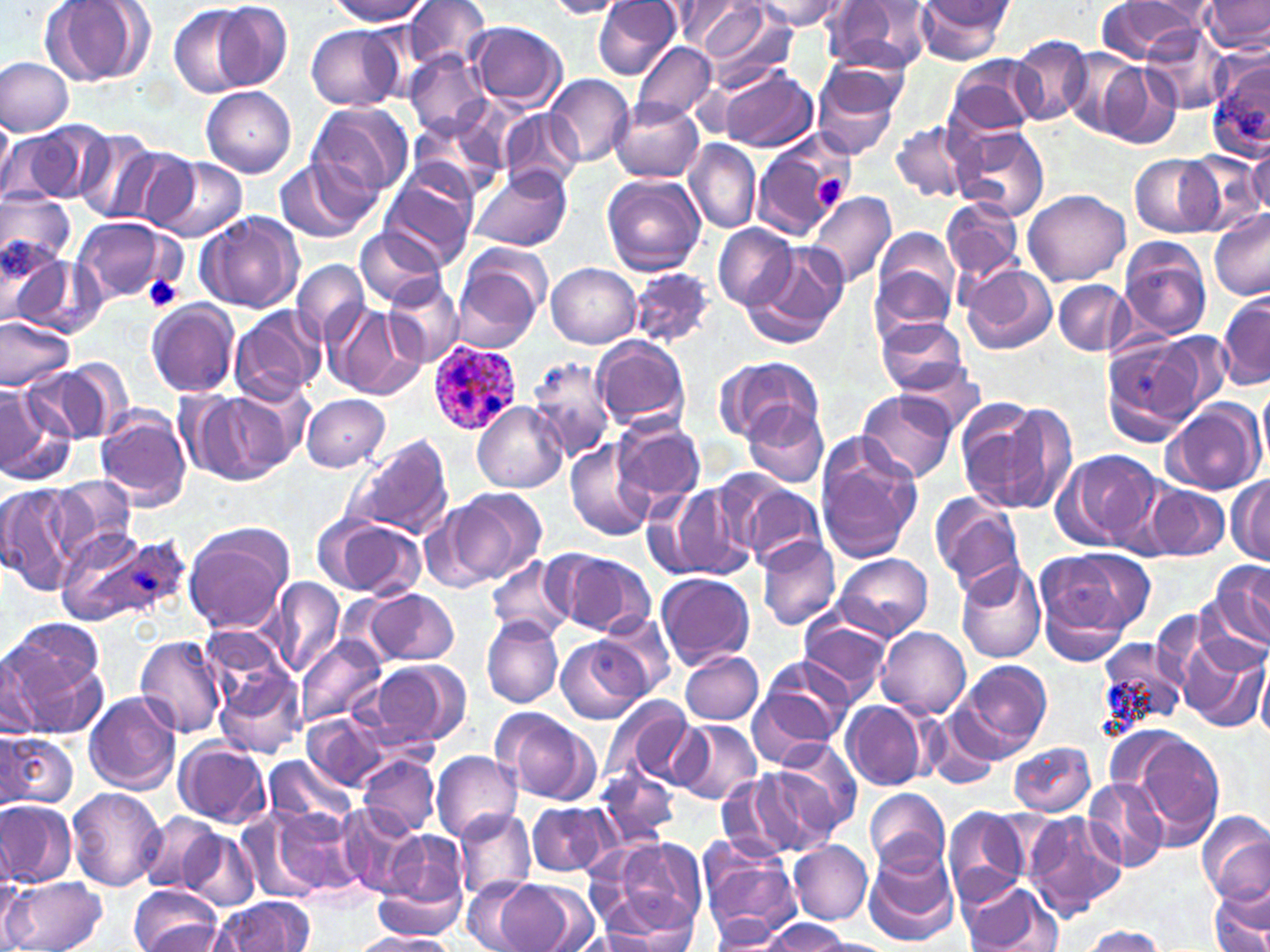
{
  "slide_level_diagnosis": "Plasmodium ovale",
  "modality": "optical microscopy",
  "uninfected_red_blood_cell_locations": "approximate bounding boxes as (x1, y1, x2, y2) in pixels: (204, 0, 293, 90), (327, 0, 431, 25), (403, 0, 491, 69), (753, 0, 847, 30), (821, 0, 930, 76), (913, 0, 1014, 65), (1203, 0, 1269, 53), (39, 1, 154, 86), (543, 1, 634, 18), (593, 1, 680, 79), (666, 2, 764, 51), (1095, 2, 1201, 61), (696, 3, 795, 86), (169, 5, 259, 97), (467, 20, 567, 110), (305, 24, 407, 111), (1141, 24, 1231, 115), (1011, 37, 1094, 124), (632, 40, 720, 123), (819, 50, 912, 121), (1062, 50, 1148, 137), (405, 51, 490, 139), (1207, 52, 1270, 158), (945, 55, 1044, 139), (0, 57, 72, 137), (1086, 59, 1181, 148), (721, 65, 818, 151), (812, 71, 902, 161), (545, 75, 633, 168), (201, 85, 297, 178), (308, 100, 414, 200), (610, 100, 703, 183), (501, 109, 582, 193), (0, 111, 14, 197), (407, 113, 507, 199), (891, 119, 974, 203), (2, 123, 104, 205), (952, 125, 1050, 222), (73, 129, 163, 225), (753, 132, 857, 239), (1246, 136, 1270, 219), (685, 139, 760, 233), (109, 143, 198, 230), (1186, 153, 1264, 235), (1130, 154, 1222, 237), (152, 158, 246, 244), (274, 159, 370, 243), (380, 164, 479, 267), (469, 165, 571, 254), (601, 174, 707, 275), (1023, 188, 1132, 285), (1, 192, 74, 272), (806, 192, 896, 287), (943, 197, 1022, 284), (948, 202, 1035, 353), (1208, 209, 1270, 302), (196, 212, 304, 313), (73, 216, 177, 305), (714, 223, 799, 311), (873, 227, 962, 328), (355, 228, 447, 307), (1119, 237, 1213, 342), (2, 241, 75, 332), (741, 242, 849, 348), (452, 250, 549, 352), (18, 257, 107, 340), (293, 259, 371, 348), (547, 263, 641, 348), (959, 264, 1057, 355), (630, 267, 715, 347), (385, 276, 465, 367), (1054, 280, 1131, 357), (1216, 292, 1270, 390), (145, 300, 240, 398), (327, 304, 426, 401), (229, 306, 325, 405), (0, 315, 75, 390), (873, 316, 970, 395), (1153, 333, 1238, 409), (592, 335, 691, 430), (1104, 339, 1200, 444), (527, 354, 615, 461), (715, 354, 823, 444), (60, 355, 134, 440), (893, 361, 988, 435), (26, 365, 114, 444), (0, 384, 68, 483), (856, 390, 959, 484), (188, 392, 292, 484), (301, 395, 390, 472), (955, 397, 1070, 517), (1161, 399, 1265, 497), (472, 401, 567, 493), (744, 402, 829, 488), (96, 411, 192, 510), (611, 418, 705, 511), (348, 434, 454, 542), (813, 435, 923, 564), (565, 442, 654, 542), (1054, 449, 1162, 550), (1228, 474, 1269, 564), (45, 476, 137, 566), (729, 478, 825, 568), (0, 481, 78, 594), (658, 483, 758, 583), (1145, 483, 1229, 561), (444, 488, 546, 586), (931, 493, 1026, 593), (320, 516, 426, 600), (184, 523, 295, 634), (756, 535, 842, 631), (548, 550, 657, 638), (1032, 550, 1144, 659), (834, 552, 933, 641), (487, 559, 573, 640), (955, 559, 1047, 663), (1210, 563, 1269, 650), (656, 572, 755, 670), (264, 578, 346, 679), (362, 588, 459, 666), (594, 611, 677, 699), (798, 611, 895, 701), (481, 615, 563, 708), (876, 626, 970, 717), (1180, 630, 1266, 731), (135, 635, 228, 738), (294, 635, 387, 731), (1096, 636, 1189, 735), (556, 637, 648, 723), (4, 640, 108, 741), (4, 649, 48, 739), (680, 651, 765, 725), (753, 657, 855, 749), (1255, 657, 1270, 740), (367, 659, 471, 749), (951, 659, 1053, 762), (215, 663, 308, 760), (747, 689, 840, 770), (84, 692, 182, 794), (598, 694, 697, 792), (842, 701, 929, 791), (492, 707, 601, 806), (919, 709, 1001, 792), (302, 714, 388, 791), (669, 720, 764, 806), (1128, 731, 1225, 845), (0, 732, 76, 812), (768, 738, 861, 840), (174, 741, 271, 829), (1009, 742, 1097, 817), (431, 750, 523, 842), (359, 754, 438, 836), (262, 756, 357, 832), (596, 766, 679, 849), (719, 769, 831, 861), (1083, 778, 1170, 874), (67, 787, 166, 891), (867, 788, 950, 877), (0, 800, 76, 888), (527, 800, 613, 878), (256, 804, 364, 901), (337, 805, 426, 898), (942, 807, 1032, 907), (453, 811, 536, 901), (1021, 811, 1126, 920), (140, 813, 222, 894), (1197, 814, 1270, 906), (178, 827, 257, 908), (376, 827, 470, 923), (603, 835, 708, 935), (788, 839, 873, 925), (697, 840, 799, 940), (862, 845, 960, 947), (462, 876, 539, 952), (3, 877, 109, 952), (372, 877, 468, 939), (495, 879, 591, 952), (958, 879, 1054, 952), (1207, 883, 1269, 952), (129, 887, 226, 952), (592, 896, 698, 952), (209, 897, 311, 951), (708, 911, 789, 947), (759, 918, 852, 950), (1080, 925, 1166, 951), (350, 931, 458, 952)",
  "magnification": "1000x",
  "image_size": "1270×952 pixels",
  "plasmodium_ovale_infected_red_blood_cell_locations": "approximate bounding boxes as (x1, y1, x2, y2) in pixels: (430, 339, 520, 433), (56, 524, 185, 630)",
  "stain": "May-Grünwald-Giemsa",
  "preparation": "thin blood film",
  "platelet_locations": "approximate bounding boxes as (x1, y1, x2, y2) in pixels: (813, 170, 851, 210), (144, 275, 184, 314)",
  "field_of_view": "single"
}